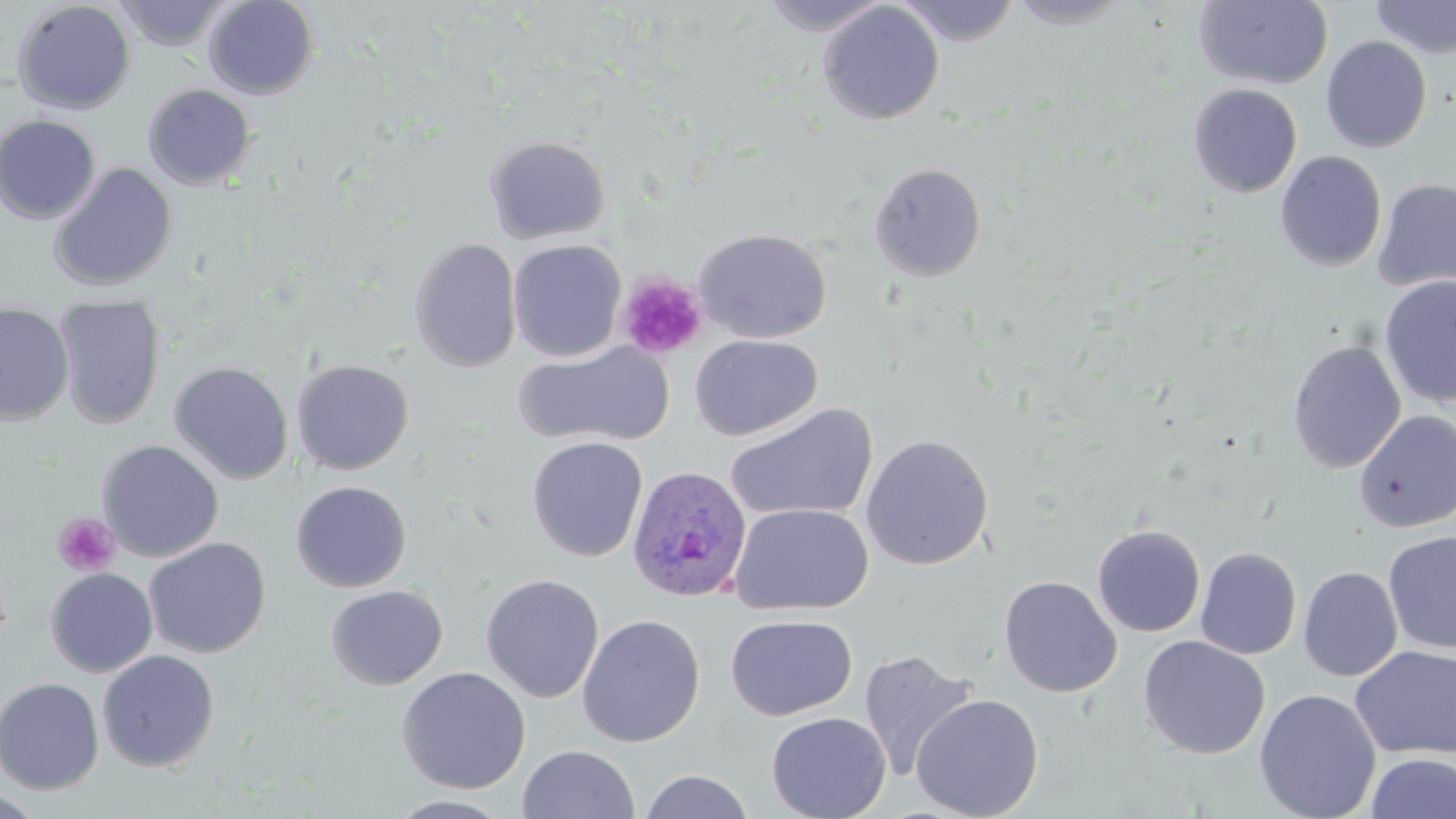

Approximate bounding boxes as named x1/y1/x2/y2 corners in pixels. Plasmodium ovale-infected red blood cell locations: (x1=626, y1=464, x2=753, y2=602). Uninfected red blood cell locations: (x1=203, y1=0, x2=318, y2=99), (x1=760, y1=0, x2=892, y2=36), (x1=896, y1=0, x2=1022, y2=45), (x1=1006, y1=0, x2=1136, y2=29), (x1=1369, y1=0, x2=1456, y2=60), (x1=12, y1=1, x2=136, y2=116), (x1=113, y1=1, x2=232, y2=52), (x1=1194, y1=1, x2=1333, y2=89), (x1=818, y1=2, x2=944, y2=125), (x1=1321, y1=36, x2=1432, y2=153), (x1=1188, y1=83, x2=1302, y2=197), (x1=143, y1=84, x2=256, y2=190), (x1=0, y1=115, x2=101, y2=224), (x1=484, y1=135, x2=611, y2=244), (x1=1275, y1=150, x2=1387, y2=272), (x1=868, y1=162, x2=987, y2=282), (x1=48, y1=163, x2=178, y2=292), (x1=1372, y1=178, x2=1456, y2=292), (x1=694, y1=228, x2=832, y2=343), (x1=408, y1=238, x2=523, y2=373), (x1=508, y1=239, x2=627, y2=362), (x1=1379, y1=274, x2=1456, y2=408), (x1=54, y1=296, x2=166, y2=430), (x1=0, y1=303, x2=74, y2=425), (x1=689, y1=334, x2=822, y2=440), (x1=1286, y1=339, x2=1406, y2=473), (x1=513, y1=341, x2=674, y2=450), (x1=292, y1=358, x2=414, y2=475), (x1=168, y1=361, x2=294, y2=485), (x1=725, y1=403, x2=878, y2=522), (x1=1354, y1=410, x2=1456, y2=533), (x1=860, y1=434, x2=994, y2=570), (x1=527, y1=436, x2=648, y2=562), (x1=96, y1=439, x2=224, y2=562), (x1=290, y1=480, x2=412, y2=592), (x1=728, y1=502, x2=874, y2=615), (x1=1092, y1=524, x2=1206, y2=637), (x1=1383, y1=530, x2=1456, y2=656), (x1=143, y1=537, x2=271, y2=658), (x1=1195, y1=547, x2=1302, y2=660), (x1=1298, y1=566, x2=1402, y2=682), (x1=45, y1=567, x2=158, y2=677), (x1=481, y1=573, x2=604, y2=704), (x1=999, y1=576, x2=1123, y2=698), (x1=325, y1=585, x2=448, y2=690), (x1=577, y1=614, x2=705, y2=748), (x1=725, y1=614, x2=857, y2=721), (x1=1138, y1=635, x2=1270, y2=759), (x1=1350, y1=645, x2=1456, y2=760), (x1=857, y1=649, x2=978, y2=781), (x1=97, y1=650, x2=220, y2=772), (x1=396, y1=666, x2=531, y2=794), (x1=0, y1=673, x2=220, y2=786), (x1=0, y1=677, x2=104, y2=794), (x1=1254, y1=688, x2=1381, y2=819), (x1=910, y1=693, x2=1045, y2=819), (x1=765, y1=711, x2=891, y2=819), (x1=518, y1=744, x2=640, y2=818), (x1=1365, y1=753, x2=1456, y2=819), (x1=638, y1=770, x2=755, y2=819), (x1=0, y1=789, x2=45, y2=817), (x1=385, y1=795, x2=517, y2=818). Platelet locations: (x1=617, y1=273, x2=707, y2=361), (x1=52, y1=513, x2=120, y2=576). Slide-level diagnosis: Plasmodium ovale. Thin blood film. 1000x magnification. Image is 1456×819 pixels. Single field of view. Optical microscopy. May-Grünwald-Giemsa stain.